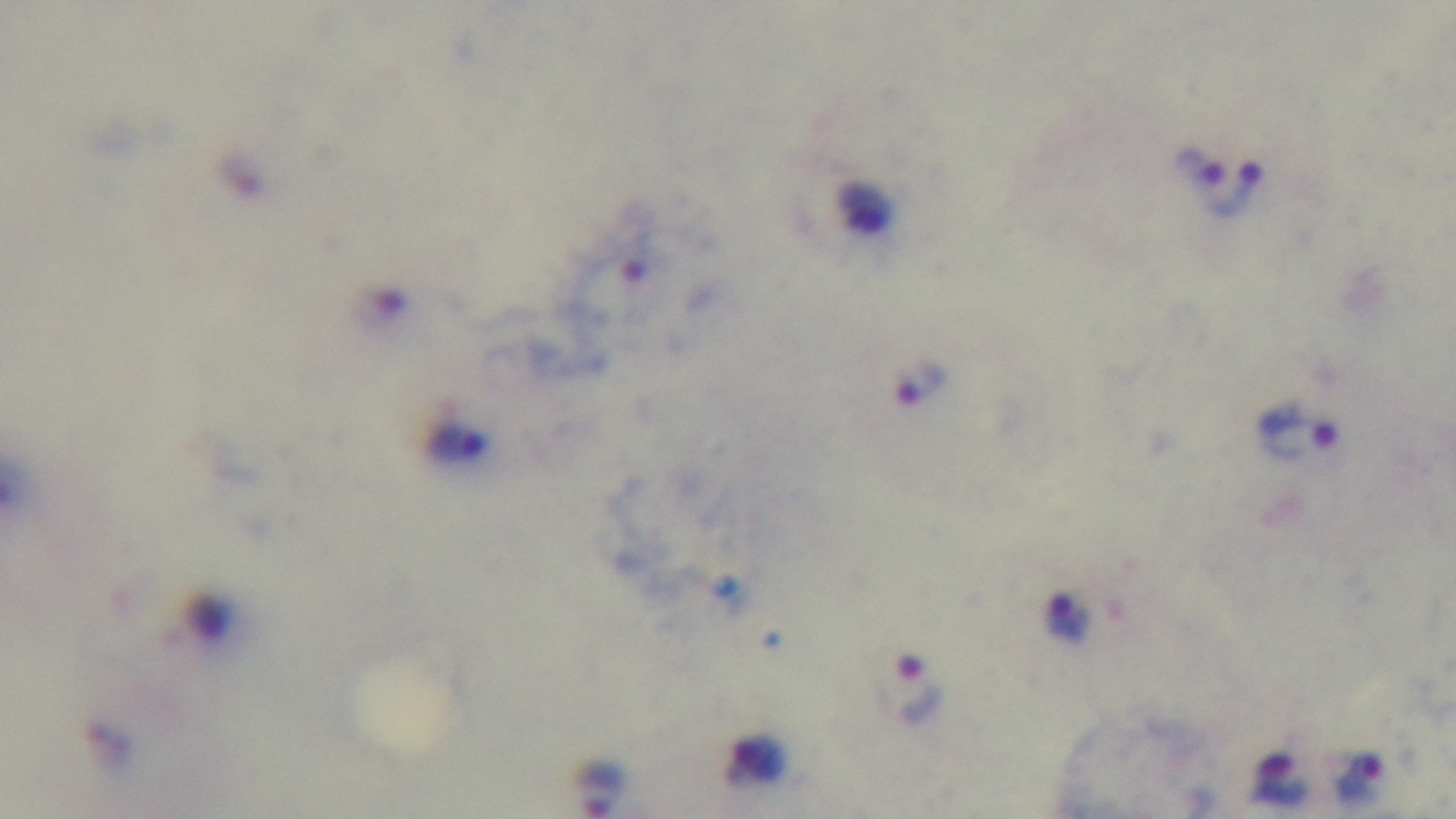

{
  "preparation": "thick",
  "malaria_status": "infected",
  "objective": "100x oil immersion",
  "capture": "mounted 4K digital camera",
  "modality": "light microscopy",
  "stain": "Giemsa",
  "field_of_view": "single"
}